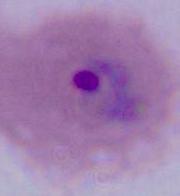
Summary:
  - Modality: photomicrograph
  - Magnification: 400x or 1000x
  - Identification: Plasmodium